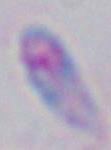
identification = Toxoplasma gondii
modality = micrograph
magnification = 1000x